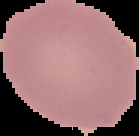

preparation = thin blood film
image type = segmented cell region with the area outside set to black
malaria status = uninfected
image size = 139×136 pixels